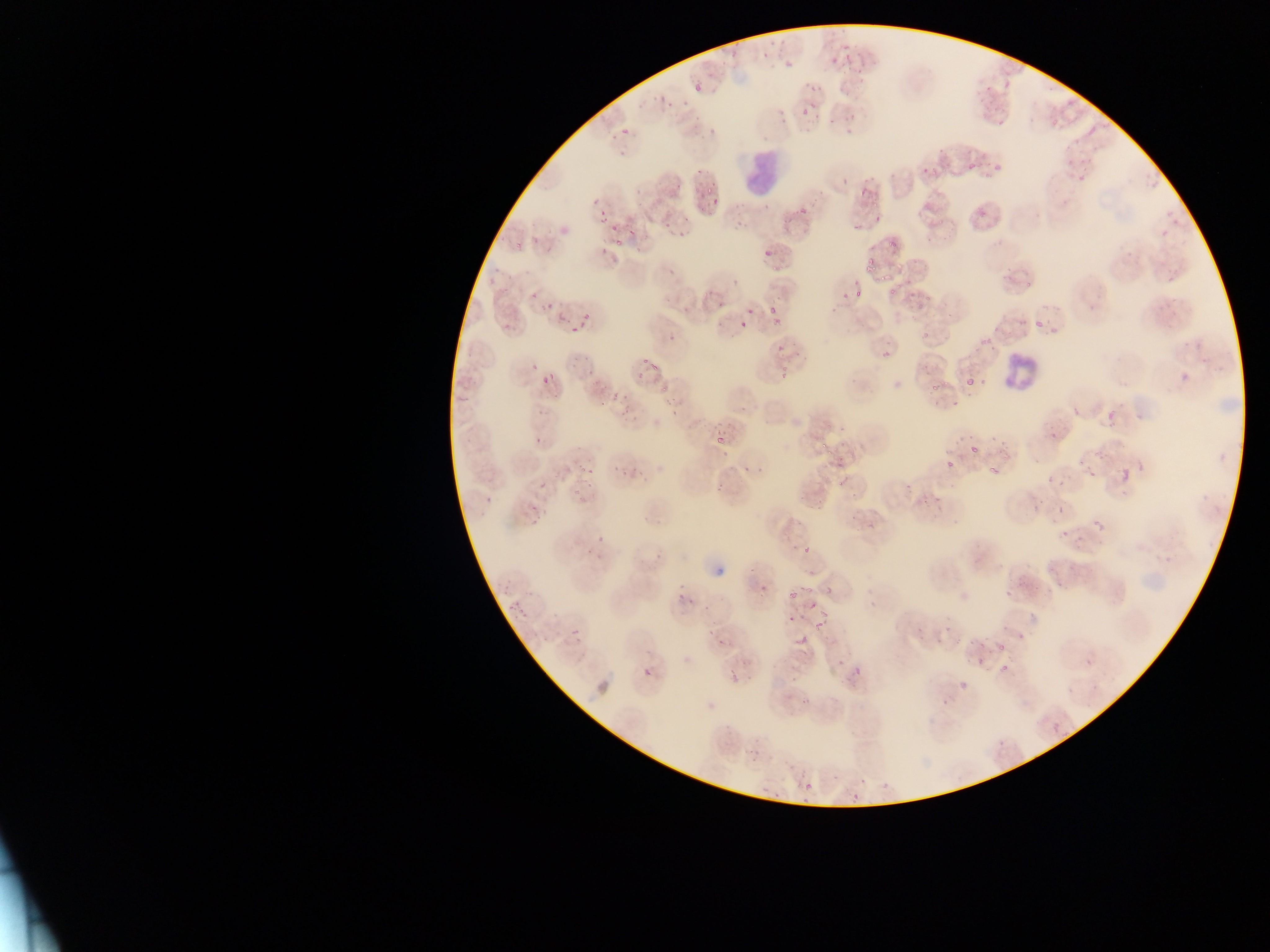 Approximate bounding boxes as left top right bottom in pixels. Malaria parasite locations: 757 23 790 55; 830 40 869 79; 717 43 739 63; 772 49 793 69; 690 76 704 98; 803 76 826 98; 651 98 676 116; 796 98 818 126; 828 108 857 128; 621 127 631 136; 1088 128 1095 136; 1055 153 1080 167; 990 159 1007 176; 915 162 930 180; 969 163 977 172; 695 168 704 176; 1075 171 1086 180; 839 174 852 189; 860 179 873 195; 699 186 720 196; 1164 189 1189 224; 588 191 603 209; 706 198 724 207; 794 201 812 215; 592 208 607 222; 661 218 672 233; 852 218 865 236; 625 221 642 238; 603 222 616 234; 1159 224 1172 241; 508 230 531 252; 888 234 901 246; 613 236 630 247; 758 248 773 260; 862 254 876 267; 859 261 874 274; 658 264 684 282; 1160 269 1176 282; 726 270 744 290; 875 274 885 287; 1017 274 1036 293; 913 277 938 298; 884 284 898 300; 531 287 538 299; 854 288 864 297; 1165 289 1181 306; 841 292 850 301; 540 299 553 308; 714 299 723 314; 745 303 753 318; 766 305 775 312; 578 309 596 325; 769 314 783 325; 1030 316 1046 333; 568 322 585 335; 738 322 748 331; 664 330 682 348; 918 330 929 338; 974 330 994 356; 775 344 786 357; 880 347 894 360; 564 353 596 378; 634 354 665 376; 529 358 541 372; 1175 366 1195 387; 549 371 556 380; 540 375 548 384; 966 377 975 385; 927 385 938 393; 597 388 622 406; 660 393 688 415; 1103 405 1121 426; 1067 407 1083 420; 1044 422 1062 444; 713 430 729 450; 533 432 547 447; 821 438 828 447; 991 438 1008 451; 818 440 844 468; 967 442 984 461; 943 460 957 469; 984 462 1002 483; 1116 463 1131 485; 575 464 594 473; 742 464 752 474; 756 466 763 474; 1085 467 1098 481; 608 468 634 480; 832 472 850 487; 584 476 601 490; 1047 476 1055 484; 539 480 548 491; 716 481 723 491; 904 484 912 492; 922 485 951 511; 479 496 490 506; 1051 500 1068 519; 526 503 536 512; 1092 506 1106 537; 529 513 540 526; 1058 527 1066 539; 596 530 607 545; 1075 534 1084 543; 801 542 810 556; 649 543 662 560; 584 546 594 558; 1054 578 1067 593; 1005 580 1018 596; 674 583 688 601; 758 583 768 592; 798 583 819 595; 825 586 832 595; 786 588 795 599; 685 598 701 607; 807 599 822 610; 507 602 514 612; 517 602 532 619; 1026 611 1037 620; 783 615 795 625; 998 620 1011 636; 813 622 831 633; 571 627 581 639; 796 633 807 646; 1015 633 1033 648; 715 638 724 648; 994 639 1010 655; 639 653 654 680; 770 656 782 669; 975 657 985 666; 1084 657 1094 667; 738 659 748 666; 852 659 867 677; 998 662 1011 673; 725 668 738 685; 745 672 756 683; 789 675 796 683; 954 680 969 688; 799 689 813 704; 938 698 951 708; 1051 724 1060 733; 747 740 766 759; 847 780 863 805; 804 781 813 790; 764 784 782 799; 796 794 813 804. Leukocyte locations: 739 149 800 200; 1004 345 1050 388. Mobile-phone photograph taken through the microscope. Collected in Ghana. Thin blood film. Image is 1270×952 pixels. One field of view.